Name the parasite shown.
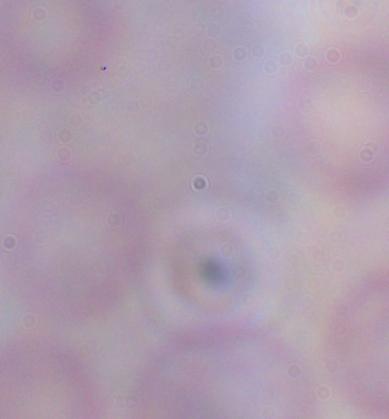
This is a trypanosome.

{
  "magnification": "1000x",
  "modality": "micrograph"
}